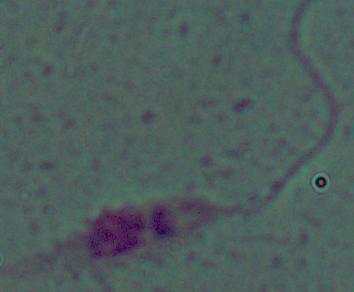

Summary:
  - Identification: Leishmania
  - Magnification: 1000x
  - Modality: micrograph